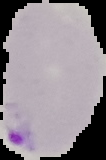 Result: malaria parasites identified. Image is 106×160 pixels. Cell region segmented out of the field of view; the surrounding area is masked to black. From a thin blood smear.